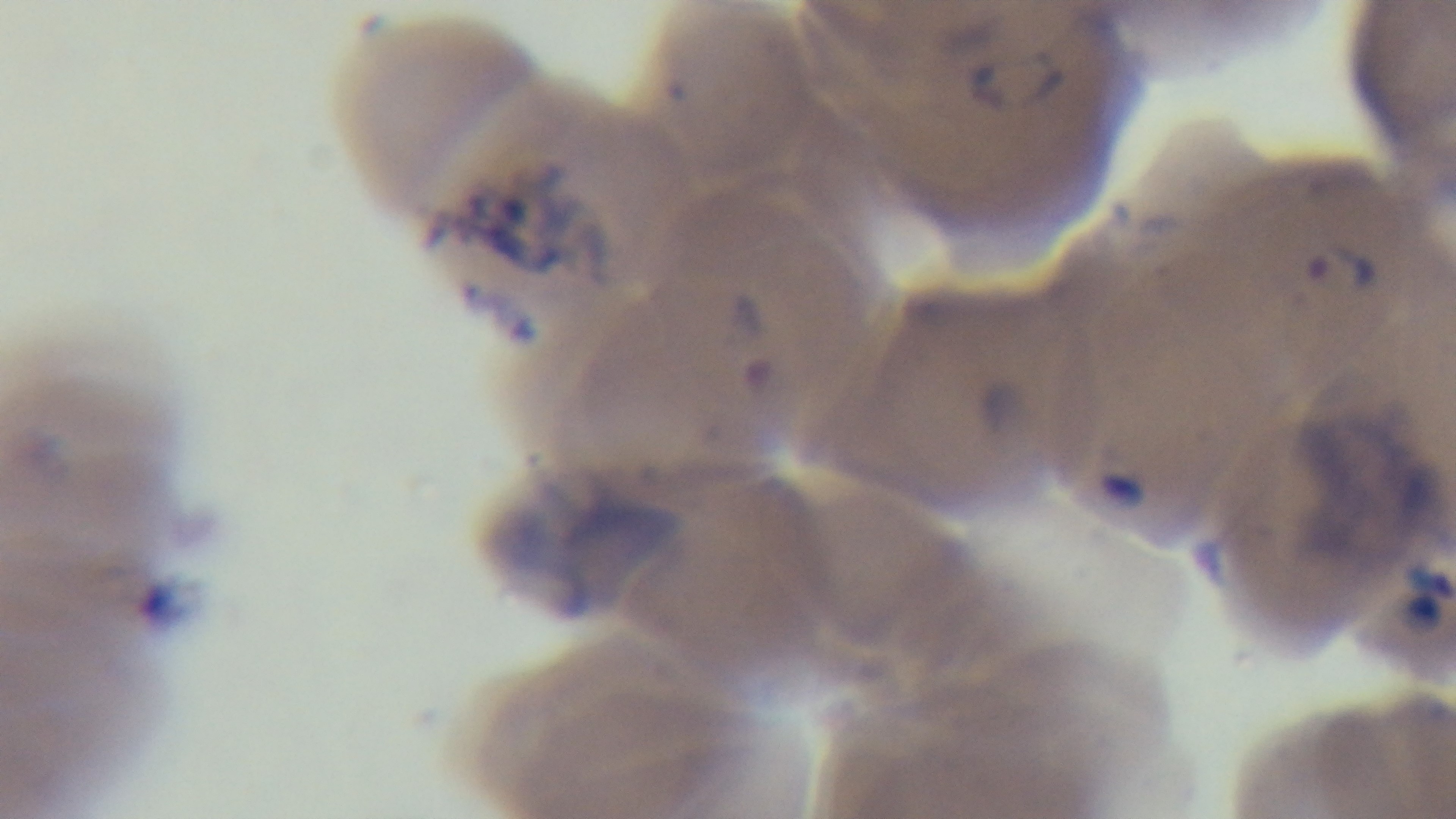
capture: mounted 4K digital camera
preparation: thin smear
stain: Giemsa
objective: 100x oil immersion
malaria_status: infected
modality: light microscopy
field_of_view: one from the slide